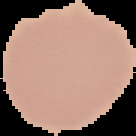
image size = 136×136 pixels
image type = segmented cell region on a black background
result = no malaria parasites detected
preparation = thin blood smear